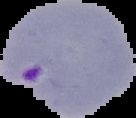

Summary:
  - Malaria status: parasitized
  - Image type: segmented cell region on a black background
  - Preparation: thin blood smear
  - Image size: 136×118 pixels